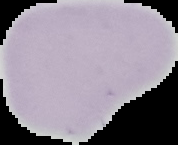

Summary:
  - Image type: cell region segmented out of the field of view; surrounding area masked to black
  - Result: no Plasmodium parasites detected
  - Preparation: thin blood film
  - Image size: 178×145 pixels